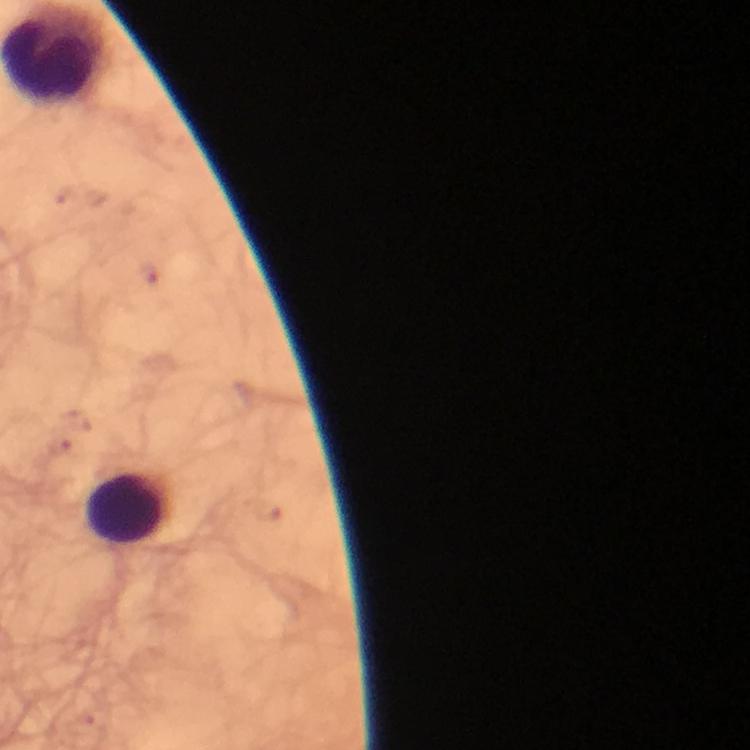
preparation = thick blood film
capture = smartphone photograph through a microscope
malaria parasites = none seen
leukocyte locations = approximate centers as (x, y) in pixels: (127, 508)
image size = 750×750 pixels
context = from a diagnostic examination for malaria
magnification = 100x
immersion oil = used
cropped from = a single field of view
stain = Giemsa